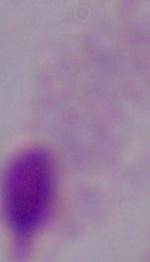 A trichomonad is shown. Photomicrograph. 1000x magnification.